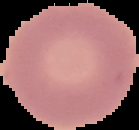
image size = 139×130 pixels
preparation = thin blood film
image type = segmented cell region with the area outside set to black
malaria status = uninfected